Locate and identify every blood parasite.
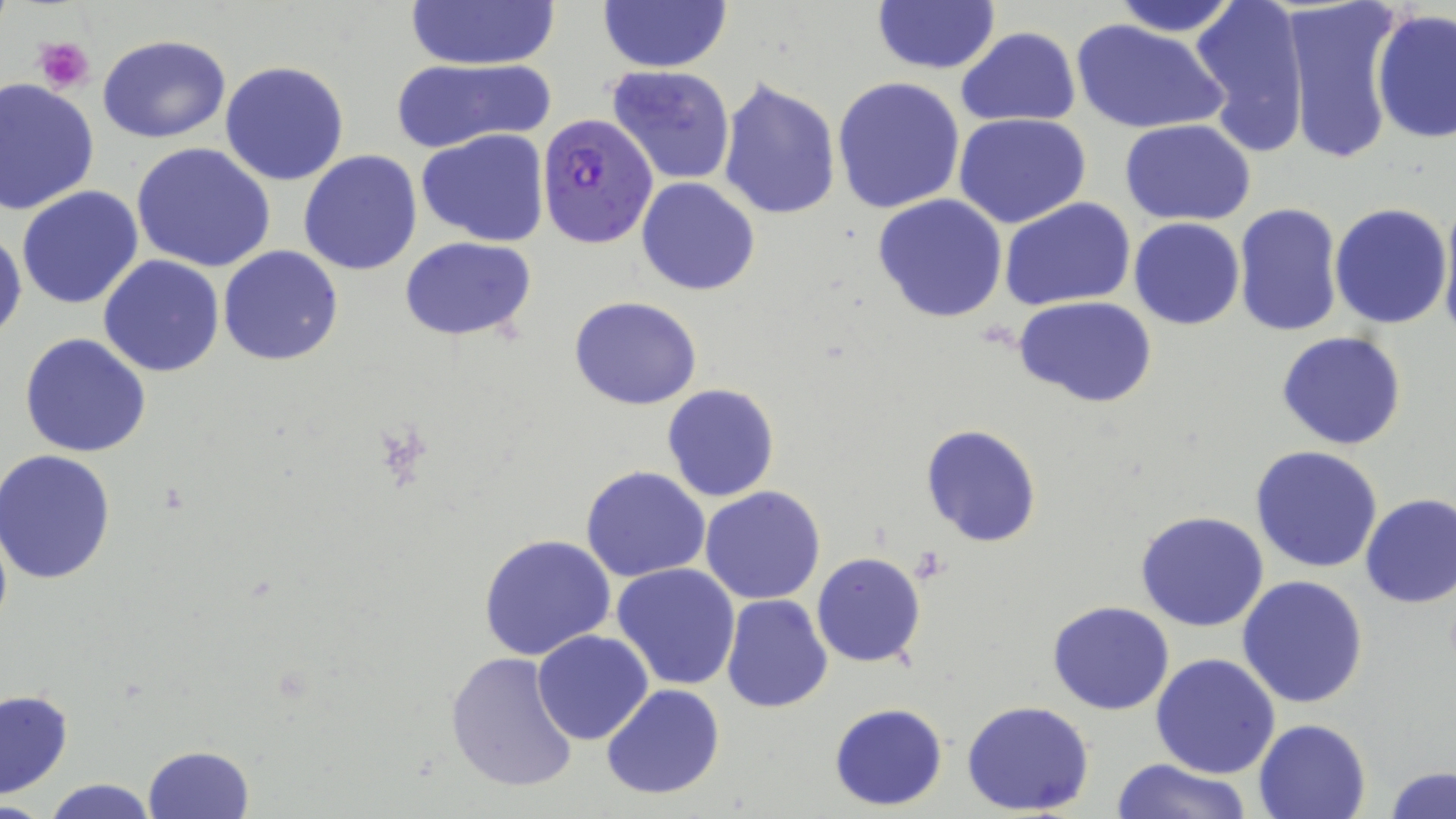

Approximate bounding boxes as named x1/y1/x2/y2 corners in pixels.
Plasmodium falciparum-infected red blood cells: (x1=534, y1=112, x2=659, y2=249).
No Plasmodium ovale, Plasmodium malariae, Plasmodium vivax, Babesia divergens, or Trypanosoma brucei observed.

slide-level diagnosis = Plasmodium falciparum
image size = 1456×819 pixels
modality = light microscopy
magnification = 1000x
platelet locations = approximate bounding boxes as named x1/y1/x2/y2 corners in pixels: (x1=34, y1=37, x2=95, y2=92)
stain = May-Grünwald-Giemsa
preparation = thin blood smear
field of view = single
uninfected red blood cell locations = approximate bounding boxes as named x1/y1/x2/y2 corners in pixels: (x1=404, y1=0, x2=559, y2=73), (x1=1107, y1=0, x2=1244, y2=38), (x1=1189, y1=0, x2=1312, y2=154), (x1=1282, y1=0, x2=1402, y2=167), (x1=597, y1=1, x2=731, y2=73), (x1=870, y1=1, x2=1001, y2=76), (x1=1372, y1=10, x2=1456, y2=143), (x1=1071, y1=19, x2=1226, y2=135), (x1=954, y1=27, x2=1082, y2=127), (x1=98, y1=33, x2=229, y2=143), (x1=389, y1=56, x2=555, y2=153), (x1=220, y1=60, x2=350, y2=187), (x1=606, y1=65, x2=736, y2=185), (x1=832, y1=76, x2=968, y2=214), (x1=716, y1=77, x2=841, y2=220), (x1=0, y1=80, x2=100, y2=214), (x1=955, y1=113, x2=1093, y2=228), (x1=1119, y1=119, x2=1257, y2=227), (x1=416, y1=129, x2=550, y2=245), (x1=131, y1=142, x2=277, y2=273), (x1=298, y1=151, x2=423, y2=275), (x1=636, y1=177, x2=761, y2=295), (x1=16, y1=186, x2=144, y2=311), (x1=873, y1=194, x2=1007, y2=324), (x1=999, y1=198, x2=1136, y2=311), (x1=1438, y1=198, x2=1456, y2=342), (x1=1232, y1=202, x2=1343, y2=338), (x1=1330, y1=203, x2=1453, y2=329), (x1=1128, y1=218, x2=1245, y2=330), (x1=0, y1=226, x2=24, y2=342), (x1=399, y1=235, x2=536, y2=341), (x1=218, y1=245, x2=343, y2=367), (x1=99, y1=254, x2=225, y2=377), (x1=570, y1=295, x2=702, y2=411), (x1=1013, y1=296, x2=1159, y2=407), (x1=1276, y1=331, x2=1407, y2=450), (x1=21, y1=333, x2=152, y2=459), (x1=662, y1=383, x2=779, y2=502), (x1=919, y1=423, x2=1043, y2=548), (x1=1251, y1=446, x2=1385, y2=574), (x1=1, y1=451, x2=116, y2=584), (x1=581, y1=466, x2=711, y2=583), (x1=699, y1=487, x2=826, y2=605), (x1=1359, y1=492, x2=1456, y2=609), (x1=1135, y1=510, x2=1269, y2=632), (x1=477, y1=533, x2=619, y2=663), (x1=811, y1=552, x2=928, y2=669), (x1=611, y1=563, x2=741, y2=690), (x1=1237, y1=574, x2=1369, y2=708), (x1=720, y1=595, x2=833, y2=713), (x1=1048, y1=601, x2=1176, y2=715), (x1=532, y1=630, x2=654, y2=745), (x1=445, y1=652, x2=580, y2=794), (x1=1151, y1=653, x2=1280, y2=777), (x1=600, y1=683, x2=726, y2=802), (x1=1, y1=688, x2=74, y2=800), (x1=961, y1=700, x2=1095, y2=816), (x1=828, y1=702, x2=948, y2=810), (x1=1253, y1=718, x2=1372, y2=819), (x1=140, y1=745, x2=255, y2=819), (x1=1114, y1=757, x2=1250, y2=819), (x1=1385, y1=766, x2=1455, y2=819), (x1=35, y1=777, x2=166, y2=819)